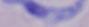
magnification: 1000x
modality: photomicrograph
identification: trypanosome